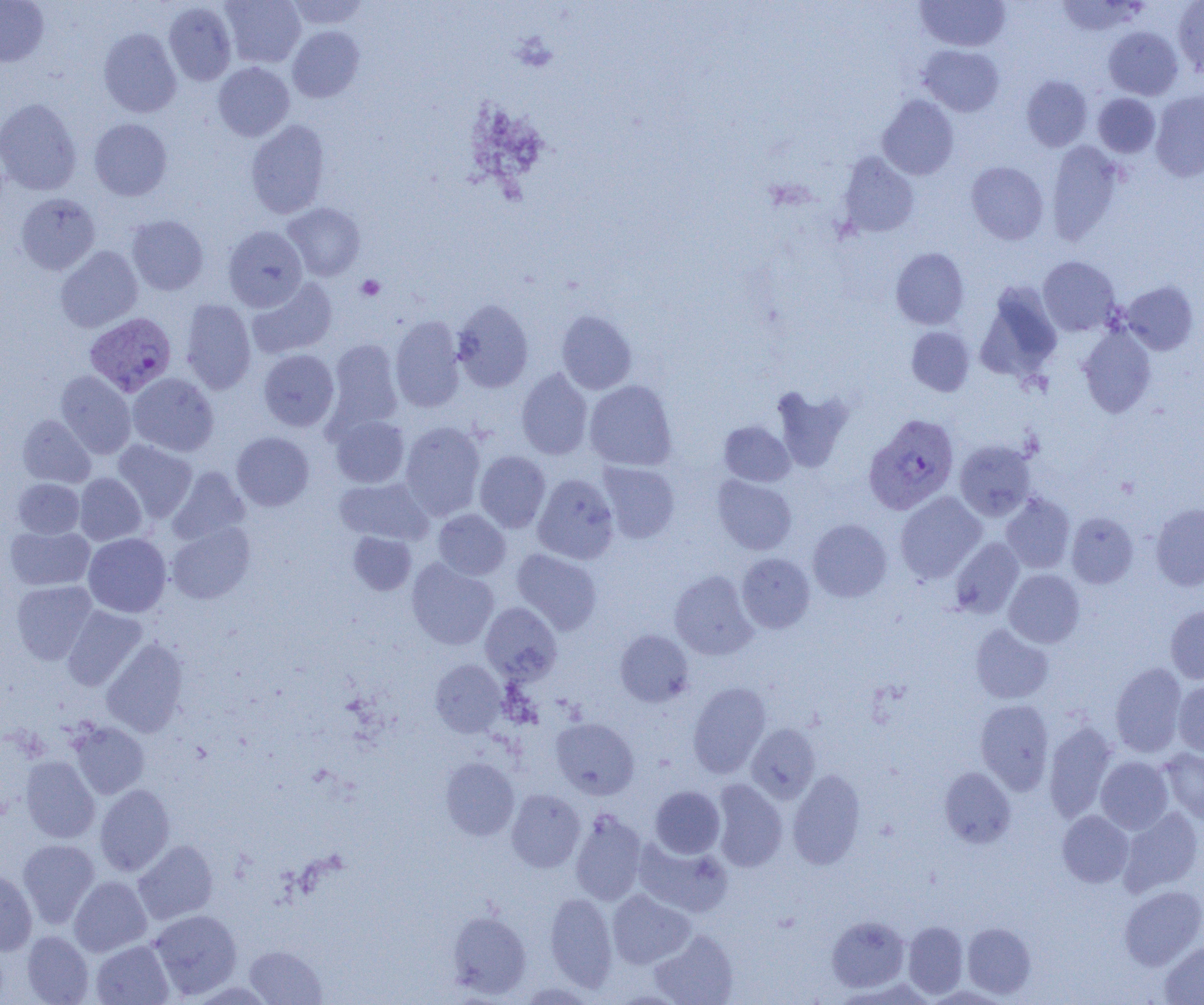 Approximate bounding boxes as named x1/y1/x2/y2 corners in pixels. Platelet locations: (x1=356, y1=275, x2=385, y2=300). Plasmodium vivax-infected red blood cell locations: (x1=85, y1=312, x2=176, y2=396), (x1=864, y1=414, x2=959, y2=515). Uninfected red blood cell locations: (x1=0, y1=0, x2=49, y2=67), (x1=220, y1=0, x2=305, y2=68), (x1=284, y1=0, x2=370, y2=29), (x1=915, y1=0, x2=1011, y2=52), (x1=1174, y1=0, x2=1204, y2=77), (x1=1056, y1=1, x2=1144, y2=37), (x1=163, y1=2, x2=236, y2=85), (x1=287, y1=26, x2=364, y2=102), (x1=1103, y1=26, x2=1183, y2=100), (x1=98, y1=28, x2=182, y2=117), (x1=918, y1=44, x2=1004, y2=116), (x1=213, y1=62, x2=294, y2=141), (x1=1021, y1=75, x2=1092, y2=151), (x1=1151, y1=90, x2=1204, y2=182), (x1=1093, y1=93, x2=1161, y2=158), (x1=877, y1=95, x2=959, y2=180), (x1=0, y1=97, x2=82, y2=194), (x1=89, y1=118, x2=172, y2=200), (x1=245, y1=119, x2=330, y2=218), (x1=1046, y1=141, x2=1124, y2=244), (x1=837, y1=152, x2=919, y2=237), (x1=966, y1=161, x2=1049, y2=244), (x1=16, y1=193, x2=100, y2=275), (x1=283, y1=203, x2=365, y2=281), (x1=126, y1=215, x2=208, y2=295), (x1=223, y1=225, x2=307, y2=311), (x1=55, y1=246, x2=143, y2=332), (x1=891, y1=247, x2=969, y2=329), (x1=1038, y1=256, x2=1120, y2=336), (x1=246, y1=278, x2=337, y2=359), (x1=1120, y1=281, x2=1199, y2=355), (x1=975, y1=282, x2=1062, y2=383), (x1=180, y1=298, x2=256, y2=394), (x1=453, y1=299, x2=533, y2=393), (x1=556, y1=310, x2=637, y2=394), (x1=390, y1=316, x2=465, y2=412), (x1=1077, y1=324, x2=1156, y2=418), (x1=906, y1=326, x2=975, y2=396), (x1=326, y1=339, x2=403, y2=431), (x1=258, y1=349, x2=339, y2=431), (x1=516, y1=368, x2=593, y2=460), (x1=56, y1=370, x2=136, y2=458), (x1=128, y1=373, x2=219, y2=456), (x1=584, y1=380, x2=677, y2=471), (x1=771, y1=386, x2=853, y2=473), (x1=18, y1=414, x2=95, y2=487), (x1=330, y1=415, x2=410, y2=488), (x1=400, y1=421, x2=486, y2=520), (x1=718, y1=421, x2=794, y2=486), (x1=232, y1=432, x2=314, y2=510), (x1=112, y1=440, x2=197, y2=522), (x1=955, y1=440, x2=1036, y2=520), (x1=474, y1=451, x2=550, y2=533), (x1=598, y1=462, x2=680, y2=544), (x1=168, y1=467, x2=250, y2=545), (x1=74, y1=473, x2=146, y2=545), (x1=533, y1=473, x2=619, y2=564), (x1=712, y1=475, x2=797, y2=555), (x1=334, y1=477, x2=433, y2=545), (x1=12, y1=478, x2=84, y2=538), (x1=895, y1=492, x2=986, y2=583), (x1=1000, y1=493, x2=1075, y2=573), (x1=1151, y1=503, x2=1204, y2=591), (x1=433, y1=509, x2=510, y2=579), (x1=1066, y1=512, x2=1139, y2=588), (x1=808, y1=519, x2=892, y2=602), (x1=167, y1=522, x2=256, y2=604), (x1=5, y1=525, x2=94, y2=590), (x1=348, y1=532, x2=416, y2=595), (x1=83, y1=533, x2=171, y2=617), (x1=950, y1=537, x2=1024, y2=618), (x1=512, y1=548, x2=602, y2=634), (x1=736, y1=553, x2=815, y2=633), (x1=407, y1=558, x2=498, y2=649), (x1=1004, y1=569, x2=1085, y2=647), (x1=669, y1=570, x2=757, y2=660), (x1=12, y1=580, x2=97, y2=664), (x1=480, y1=602, x2=562, y2=683), (x1=1165, y1=604, x2=1204, y2=684), (x1=62, y1=606, x2=147, y2=690), (x1=970, y1=624, x2=1053, y2=703), (x1=615, y1=630, x2=694, y2=706), (x1=101, y1=638, x2=189, y2=737), (x1=430, y1=659, x2=506, y2=737), (x1=1110, y1=662, x2=1187, y2=757), (x1=1173, y1=680, x2=1204, y2=757), (x1=687, y1=682, x2=771, y2=777), (x1=975, y1=699, x2=1054, y2=794), (x1=551, y1=717, x2=639, y2=799), (x1=1044, y1=720, x2=1117, y2=822), (x1=70, y1=722, x2=149, y2=799), (x1=746, y1=723, x2=820, y2=802), (x1=1161, y1=748, x2=1204, y2=826), (x1=20, y1=755, x2=99, y2=843), (x1=1096, y1=756, x2=1173, y2=833), (x1=440, y1=757, x2=519, y2=841), (x1=939, y1=767, x2=1016, y2=848), (x1=787, y1=769, x2=865, y2=869), (x1=711, y1=778, x2=787, y2=872), (x1=95, y1=784, x2=175, y2=876), (x1=650, y1=786, x2=725, y2=858), (x1=506, y1=789, x2=585, y2=872), (x1=1119, y1=807, x2=1203, y2=895), (x1=570, y1=809, x2=647, y2=905), (x1=1057, y1=810, x2=1133, y2=887), (x1=634, y1=838, x2=733, y2=917), (x1=18, y1=839, x2=99, y2=927), (x1=133, y1=840, x2=218, y2=924), (x1=0, y1=868, x2=37, y2=955), (x1=69, y1=876, x2=152, y2=956), (x1=1119, y1=885, x2=1204, y2=970), (x1=607, y1=889, x2=694, y2=968), (x1=544, y1=893, x2=617, y2=990), (x1=149, y1=909, x2=242, y2=998), (x1=447, y1=910, x2=531, y2=998), (x1=827, y1=915, x2=910, y2=993), (x1=903, y1=921, x2=968, y2=998), (x1=962, y1=922, x2=1036, y2=998), (x1=650, y1=930, x2=738, y2=1005), (x1=21, y1=931, x2=93, y2=1004), (x1=91, y1=940, x2=174, y2=1005), (x1=1159, y1=941, x2=1204, y2=1004), (x1=245, y1=945, x2=326, y2=1004). Slide-level diagnosis: Plasmodium vivax. 1000x magnification. Single field of view. Thin blood smear. Light microscopy. Image is 1204×1005 pixels.